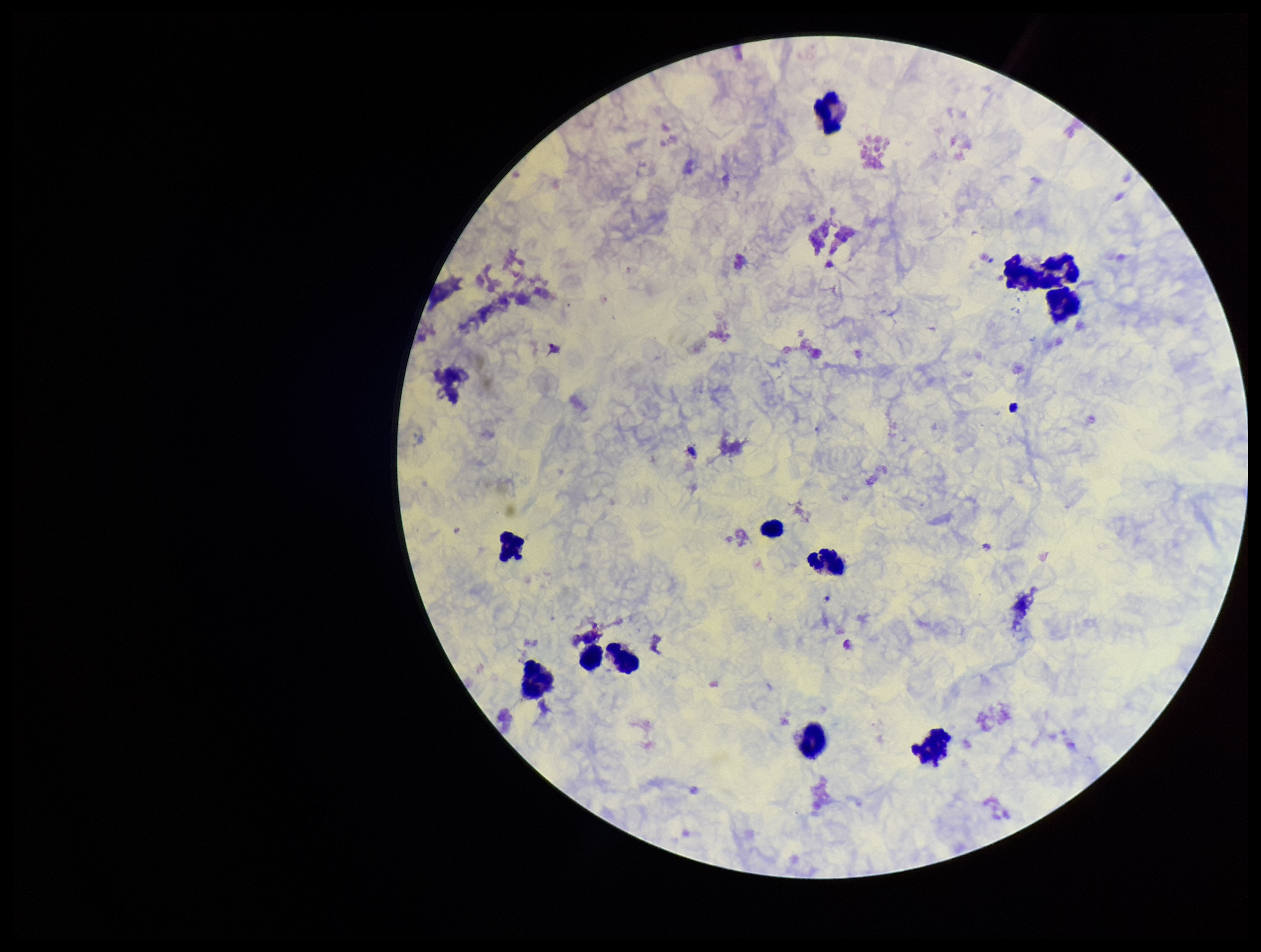
Summary:
  - Field of view: one from this slide
  - Capture: smartphone photograph through the microscope eyepiece
  - Species reported for this patient: Plasmodium vivax
  - Preparation: thick smear
  - Patient malaria status: positive
  - Parasite count: 0
  - Stain: Giemsa
  - Image size: 1261×952 pixels
  - Leukocyte count: 12
  - Plasmodium parasites: none detected